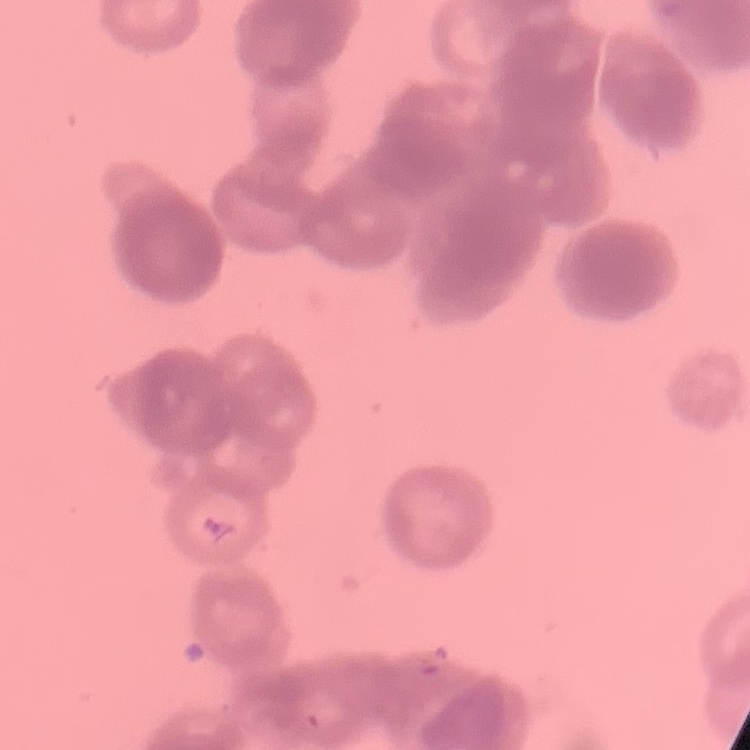 The erythrocytes show rouleaux formation. Stained with either Field's or Giemsa. Thin blood smear. One tile cut from a larger photomicrograph.